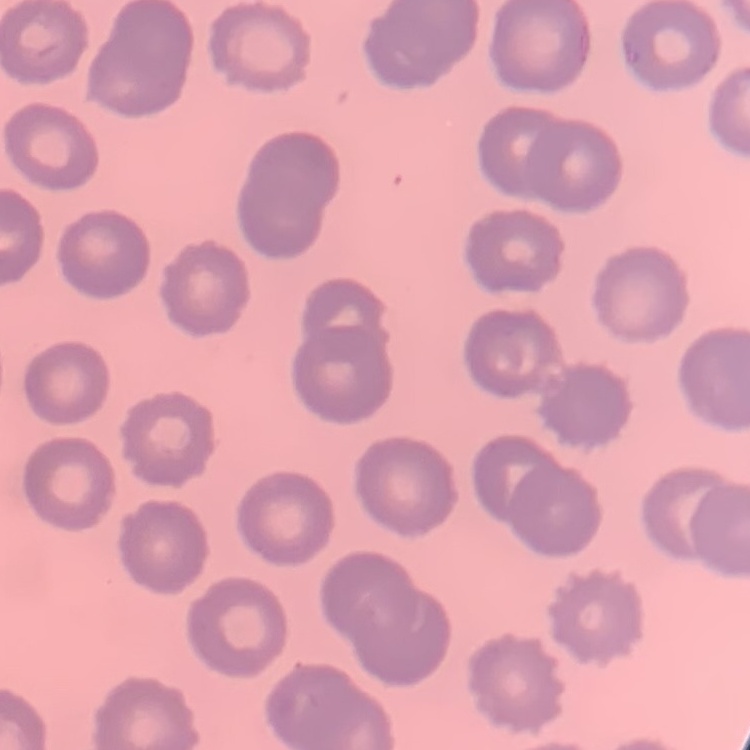
{
  "red_blood_cell_morphology": "no rouleaux formation",
  "stain": "Field's or Giemsa",
  "image_type": "one tile cut from a larger photomicrograph",
  "preparation": "thin peripheral smear"
}